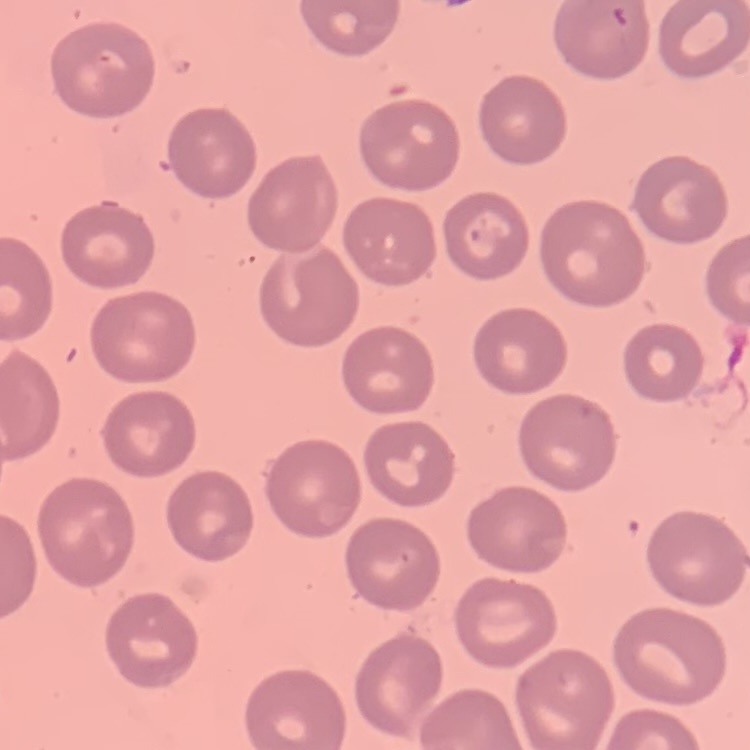 The erythrocytes show no rouleaux formation. Field's or Giemsa stain. Thin peripheral smear. Square crop of a larger photomicrograph.